Locate and identify every blood parasite.
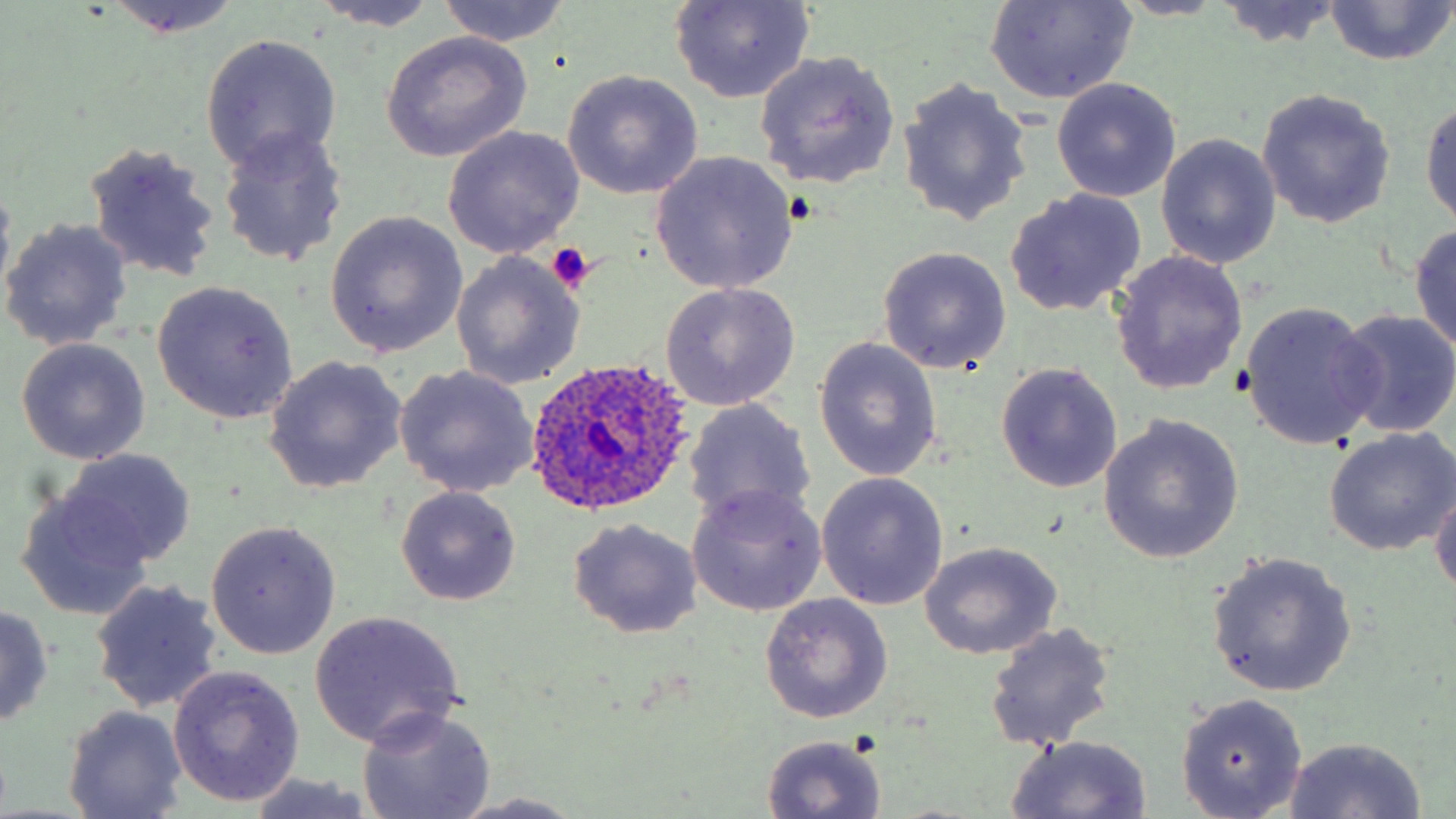

Approximate bounding boxes as named x1/y1/x2/y2 corners in pixels.
Plasmodium ovale-infected red blood cells: (x1=522, y1=359, x2=700, y2=518).
No Plasmodium falciparum, Plasmodium malariae, Plasmodium vivax, Babesia divergens, or Trypanosoma brucei observed.

slide-level diagnosis = Plasmodium ovale
modality = light microscopy
platelet locations = approximate bounding boxes as named x1/y1/x2/y2 corners in pixels: (x1=546, y1=241, x2=595, y2=293)
stain = May-Grünwald-Giemsa
field of view = single
magnification = 1000x
uninfected red blood cell locations = approximate bounding boxes as named x1/y1/x2/y2 corners in pixels: (x1=436, y1=0, x2=572, y2=47), (x1=670, y1=0, x2=817, y2=104), (x1=984, y1=0, x2=1140, y2=105), (x1=1115, y1=0, x2=1227, y2=19), (x1=97, y1=1, x2=243, y2=37), (x1=308, y1=1, x2=444, y2=33), (x1=1213, y1=1, x2=1345, y2=49), (x1=1322, y1=1, x2=1454, y2=66), (x1=380, y1=32, x2=532, y2=160), (x1=199, y1=33, x2=342, y2=174), (x1=753, y1=51, x2=901, y2=192), (x1=561, y1=71, x2=703, y2=198), (x1=897, y1=79, x2=1032, y2=228), (x1=1050, y1=80, x2=1182, y2=202), (x1=1256, y1=88, x2=1396, y2=230), (x1=1421, y1=97, x2=1456, y2=229), (x1=443, y1=126, x2=586, y2=259), (x1=217, y1=127, x2=348, y2=267), (x1=1158, y1=134, x2=1280, y2=269), (x1=81, y1=141, x2=221, y2=282), (x1=649, y1=150, x2=798, y2=295), (x1=1003, y1=190, x2=1146, y2=316), (x1=325, y1=212, x2=469, y2=358), (x1=1, y1=218, x2=133, y2=352), (x1=1409, y1=223, x2=1456, y2=358), (x1=878, y1=247, x2=1011, y2=374), (x1=1110, y1=250, x2=1249, y2=396), (x1=450, y1=253, x2=584, y2=389), (x1=152, y1=281, x2=299, y2=423), (x1=661, y1=282, x2=800, y2=410), (x1=1239, y1=301, x2=1378, y2=450), (x1=1336, y1=308, x2=1456, y2=438), (x1=15, y1=338, x2=151, y2=464), (x1=813, y1=338, x2=943, y2=482), (x1=263, y1=356, x2=407, y2=493), (x1=996, y1=363, x2=1123, y2=493), (x1=393, y1=366, x2=538, y2=500), (x1=683, y1=398, x2=817, y2=529), (x1=1099, y1=416, x2=1245, y2=565), (x1=1323, y1=428, x2=1456, y2=556), (x1=60, y1=447, x2=196, y2=568), (x1=816, y1=473, x2=949, y2=610), (x1=1430, y1=483, x2=1456, y2=601), (x1=686, y1=484, x2=827, y2=617), (x1=395, y1=486, x2=521, y2=604), (x1=13, y1=487, x2=158, y2=621), (x1=567, y1=519, x2=703, y2=638), (x1=206, y1=521, x2=341, y2=658), (x1=918, y1=541, x2=1063, y2=659), (x1=1206, y1=552, x2=1357, y2=697), (x1=89, y1=579, x2=224, y2=713), (x1=759, y1=592, x2=893, y2=723), (x1=0, y1=603, x2=55, y2=728), (x1=308, y1=611, x2=466, y2=748), (x1=984, y1=622, x2=1116, y2=750), (x1=168, y1=665, x2=303, y2=807), (x1=1176, y1=693, x2=1309, y2=818), (x1=63, y1=705, x2=189, y2=818), (x1=357, y1=707, x2=497, y2=819), (x1=761, y1=734, x2=888, y2=817), (x1=1005, y1=735, x2=1153, y2=818), (x1=1282, y1=736, x2=1427, y2=818), (x1=246, y1=773, x2=381, y2=818), (x1=450, y1=792, x2=593, y2=819)
image size = 1456×819 pixels
preparation = thin blood film